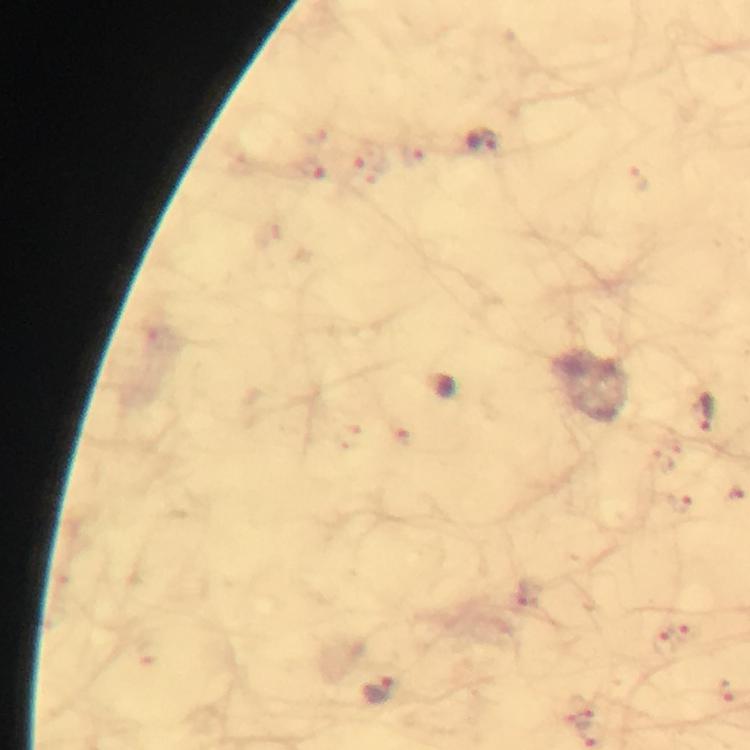
preparation: thick blood smear
malaria_parasite_locations: 'approximate centers as (x, y) in pixels: (483, 143), (705, 413), (379, 690)'
capture: smartphone mounted on the microscope
stain: Giemsa
image_size: 750×750 pixels
magnification: 100x
cropped_from: a single field of view
context: from a malaria diagnostic workup
immersion_oil: used